Report the malaria status of this cell.
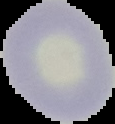
It is uninfected.

Summary:
  - Preparation: thin blood film
  - Image type: cell region segmented out of the field of view; surrounding area masked to black
  - Image size: 115×124 pixels